Identify the parasite.
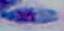
This is Toxoplasma gondii.

modality: micrograph
magnification: 1000x